Assess this cell for malaria.
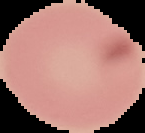

It is uninfected.

From a thin blood smear. Image is 145×133 pixels. Segmented cell region on a black background.